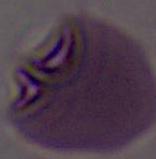

{
  "identification": "red blood cell",
  "magnification": "1000x",
  "modality": "photomicrograph"
}